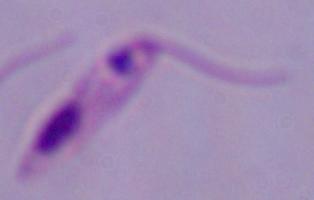

Summary:
  - Modality: micrograph
  - Identification: Leishmania
  - Magnification: 1000x